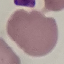
malaria status = uninfected
preparation = thin blood smear
capture = smartphone through the microscope eyepiece
stain = Giemsa
image type = automatically extracted cell patch, resized to 64 × 64 pixels